State which parasite is depicted.
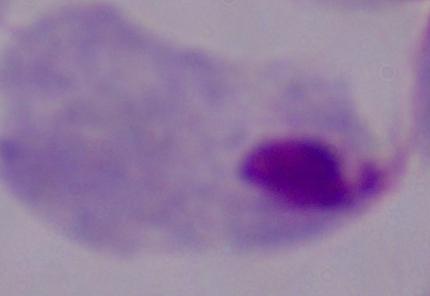

This is a trichomonad.

Summary:
  - Magnification: 1000x
  - Modality: photomicrograph